Locate every blood parasite and identify its species.
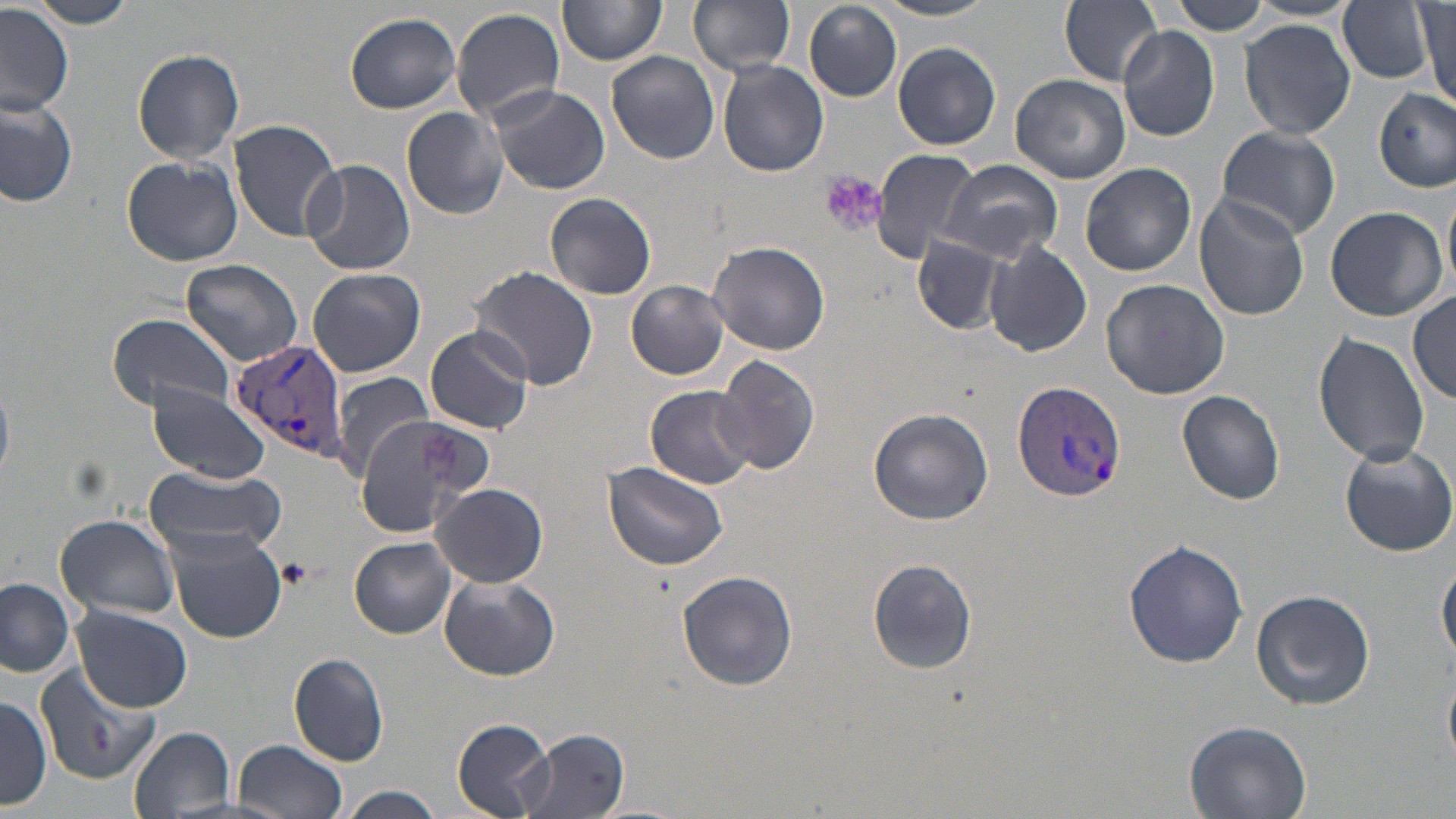
Approximate bounding boxes as named x1/y1/x2/y2 corners in pixels.
Plasmodium vivax-infected red blood cells: (x1=228, y1=339, x2=352, y2=465), (x1=1011, y1=380, x2=1127, y2=500).
No Plasmodium falciparum, Plasmodium ovale, Plasmodium malariae, Babesia divergens, or Trypanosoma brucei observed.

{
  "slide_level_diagnosis": "Plasmodium vivax",
  "preparation": "thin blood smear",
  "field_of_view": "one of a larger specimen",
  "stain": "May-Grünwald-Giemsa",
  "magnification": "1000x",
  "modality": "optical microscopy",
  "platelet_locations": "approximate bounding boxes as named x1/y1/x2/y2 corners in pixels: (x1=821, y1=170, x2=887, y2=239)",
  "image_size": "1456×819 pixels",
  "uninfected_red_blood_cell_locations": "approximate bounding boxes as named x1/y1/x2/y2 corners in pixels: (x1=24, y1=0, x2=142, y2=28), (x1=688, y1=0, x2=796, y2=76), (x1=1060, y1=0, x2=1164, y2=86), (x1=558, y1=1, x2=665, y2=68), (x1=874, y1=1, x2=998, y2=21), (x1=804, y1=2, x2=901, y2=102), (x1=1335, y1=2, x2=1439, y2=87), (x1=1165, y1=3, x2=1277, y2=35), (x1=0, y1=5, x2=73, y2=117), (x1=451, y1=6, x2=566, y2=124), (x1=1417, y1=7, x2=1454, y2=105), (x1=344, y1=12, x2=462, y2=113), (x1=1240, y1=18, x2=1355, y2=138), (x1=1117, y1=26, x2=1219, y2=142), (x1=893, y1=40, x2=1000, y2=150), (x1=132, y1=48, x2=245, y2=164), (x1=608, y1=50, x2=719, y2=164), (x1=718, y1=59, x2=827, y2=177), (x1=1009, y1=73, x2=1130, y2=184), (x1=487, y1=85, x2=611, y2=196), (x1=1375, y1=89, x2=1454, y2=190), (x1=0, y1=95, x2=79, y2=206), (x1=402, y1=106, x2=509, y2=220), (x1=227, y1=119, x2=341, y2=241), (x1=1213, y1=124, x2=1340, y2=241), (x1=867, y1=148, x2=983, y2=265), (x1=122, y1=156, x2=243, y2=267), (x1=300, y1=157, x2=415, y2=277), (x1=937, y1=160, x2=1062, y2=265), (x1=1081, y1=162, x2=1196, y2=275), (x1=546, y1=193, x2=657, y2=301), (x1=1193, y1=193, x2=1310, y2=320), (x1=1323, y1=206, x2=1448, y2=323), (x1=910, y1=233, x2=1007, y2=335), (x1=986, y1=241, x2=1092, y2=358), (x1=709, y1=242, x2=829, y2=354), (x1=181, y1=259, x2=302, y2=364), (x1=470, y1=266, x2=595, y2=391), (x1=308, y1=267, x2=425, y2=378), (x1=1102, y1=279, x2=1230, y2=399), (x1=626, y1=281, x2=731, y2=380), (x1=1409, y1=291, x2=1456, y2=404), (x1=108, y1=312, x2=235, y2=413), (x1=424, y1=324, x2=535, y2=435), (x1=1314, y1=330, x2=1430, y2=467), (x1=714, y1=354, x2=820, y2=477), (x1=330, y1=371, x2=435, y2=482), (x1=147, y1=384, x2=271, y2=486), (x1=648, y1=385, x2=759, y2=489), (x1=1178, y1=390, x2=1285, y2=504), (x1=357, y1=406, x2=486, y2=536), (x1=869, y1=409, x2=993, y2=524), (x1=1339, y1=441, x2=1456, y2=557), (x1=604, y1=460, x2=728, y2=569), (x1=142, y1=463, x2=290, y2=558), (x1=433, y1=483, x2=550, y2=585), (x1=54, y1=514, x2=180, y2=620), (x1=165, y1=523, x2=288, y2=642), (x1=350, y1=537, x2=458, y2=638), (x1=1124, y1=540, x2=1248, y2=668), (x1=867, y1=557, x2=978, y2=674), (x1=1437, y1=559, x2=1456, y2=668), (x1=677, y1=571, x2=798, y2=691), (x1=439, y1=574, x2=559, y2=682), (x1=2, y1=580, x2=74, y2=680), (x1=1251, y1=589, x2=1375, y2=711), (x1=72, y1=605, x2=193, y2=712), (x1=288, y1=652, x2=389, y2=765), (x1=34, y1=663, x2=160, y2=785), (x1=1444, y1=674, x2=1456, y2=767), (x1=0, y1=695, x2=50, y2=809), (x1=1183, y1=718, x2=1311, y2=818), (x1=453, y1=719, x2=555, y2=817), (x1=130, y1=727, x2=237, y2=817), (x1=518, y1=729, x2=631, y2=819), (x1=233, y1=739, x2=348, y2=819), (x1=329, y1=788, x2=452, y2=819)"
}